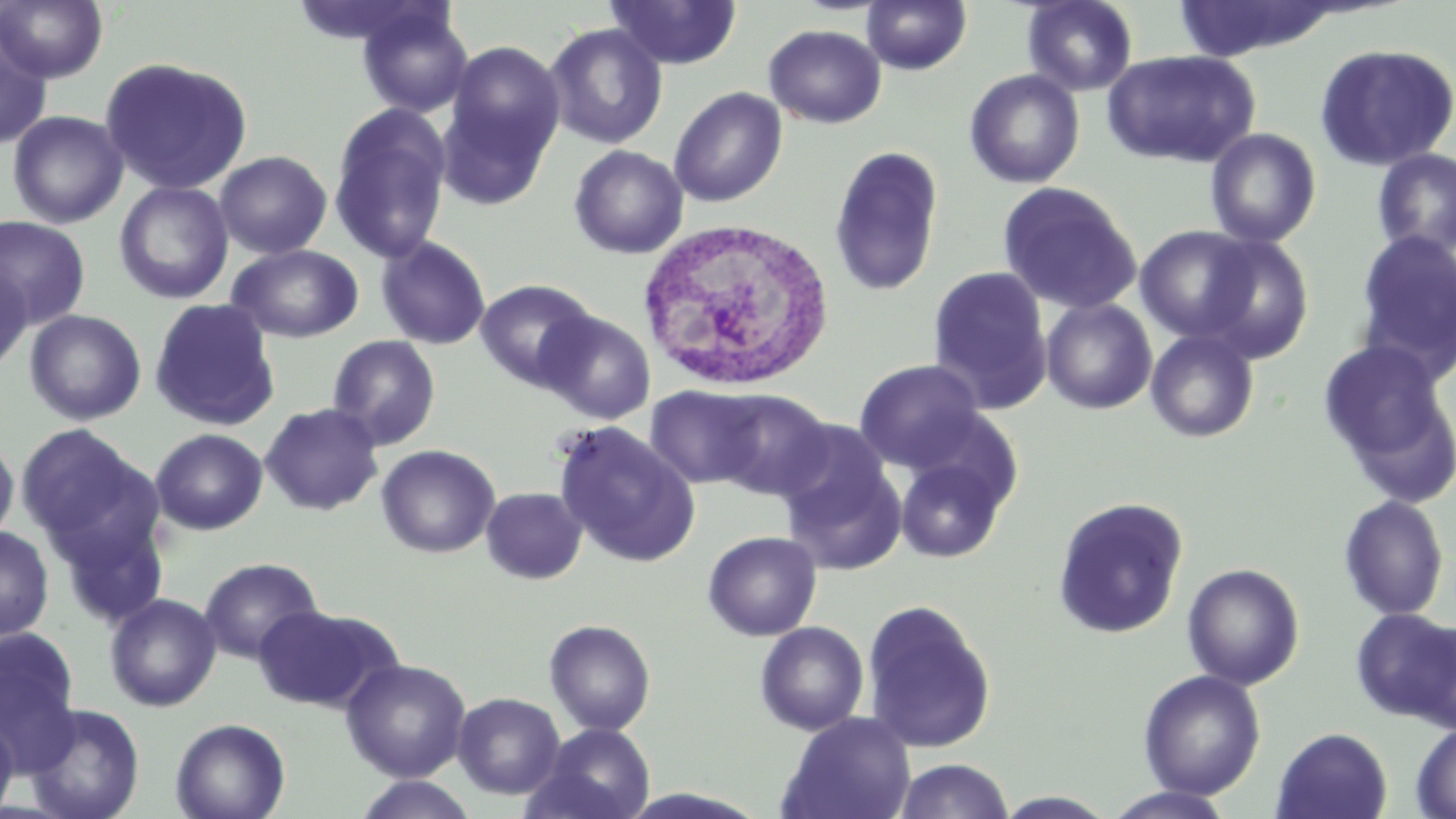

Approximate bounding boxes as (x1, y1, x2, y2) in pixels. Uninfected red blood cell locations: (0, 0, 109, 83), (605, 0, 742, 70), (862, 0, 971, 75), (1022, 0, 1138, 96), (287, 1, 438, 51), (357, 4, 474, 118), (0, 17, 53, 151), (543, 23, 668, 149), (763, 24, 887, 128), (445, 41, 565, 169), (1314, 43, 1456, 170), (1103, 50, 1260, 169), (100, 56, 253, 195), (964, 70, 1085, 189), (669, 86, 787, 207), (436, 91, 555, 209), (328, 103, 452, 264), (7, 110, 128, 228), (1205, 128, 1321, 247), (568, 144, 689, 259), (828, 145, 944, 297), (1371, 148, 1456, 259), (214, 150, 332, 259), (114, 181, 233, 304), (997, 181, 1141, 315), (0, 216, 90, 328), (1135, 225, 1263, 342), (1353, 228, 1456, 380), (1194, 234, 1315, 362), (376, 236, 491, 350), (226, 244, 364, 343), (0, 258, 32, 374), (927, 265, 1054, 415), (475, 279, 597, 390), (149, 298, 280, 431), (1041, 298, 1157, 414), (24, 309, 146, 425), (537, 310, 655, 424), (1145, 329, 1260, 443), (327, 334, 441, 450), (1318, 340, 1450, 477), (853, 359, 987, 472), (646, 385, 767, 489), (707, 388, 833, 501), (260, 403, 384, 516), (152, 418, 388, 526), (553, 423, 698, 566), (18, 424, 156, 562), (151, 428, 268, 535), (776, 432, 906, 574), (0, 436, 19, 545), (376, 444, 500, 557), (894, 453, 1011, 564), (481, 486, 587, 584), (1337, 494, 1450, 621), (1052, 497, 1189, 639), (54, 513, 169, 628), (0, 526, 54, 641), (702, 531, 822, 641), (198, 557, 324, 663), (1182, 563, 1304, 690), (104, 593, 221, 711), (860, 598, 997, 753), (255, 605, 396, 712), (1351, 608, 1456, 728), (544, 619, 656, 735), (755, 621, 869, 735), (1, 629, 81, 769), (341, 658, 471, 782), (1138, 669, 1266, 800), (452, 692, 565, 799), (25, 703, 145, 819), (778, 711, 916, 819), (0, 716, 18, 818), (170, 717, 290, 819), (527, 723, 656, 819), (1411, 723, 1456, 818), (1272, 727, 1392, 819), (893, 759, 1014, 819), (352, 775, 479, 818), (1104, 786, 1239, 819), (992, 791, 1120, 818). White blood cell locations: (635, 216, 837, 394). Slide-level diagnosis: no evidence of blood parasites. One field of a larger specimen. May-Grünwald-Giemsa stain. Image is 1456×819 pixels. Optical microscopy. 1000x magnification. Thin blood film.